Classify this cell by malaria status.
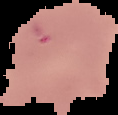
It is uninfected.

Summary:
  - Image type: segmented cell region with the area outside set to black
  - Image size: 118×115 pixels
  - Preparation: thin blood film